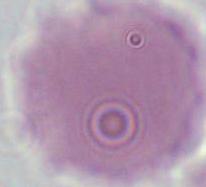

Summary:
  - Identification: erythrocyte
  - Magnification: 1000x
  - Modality: micrograph